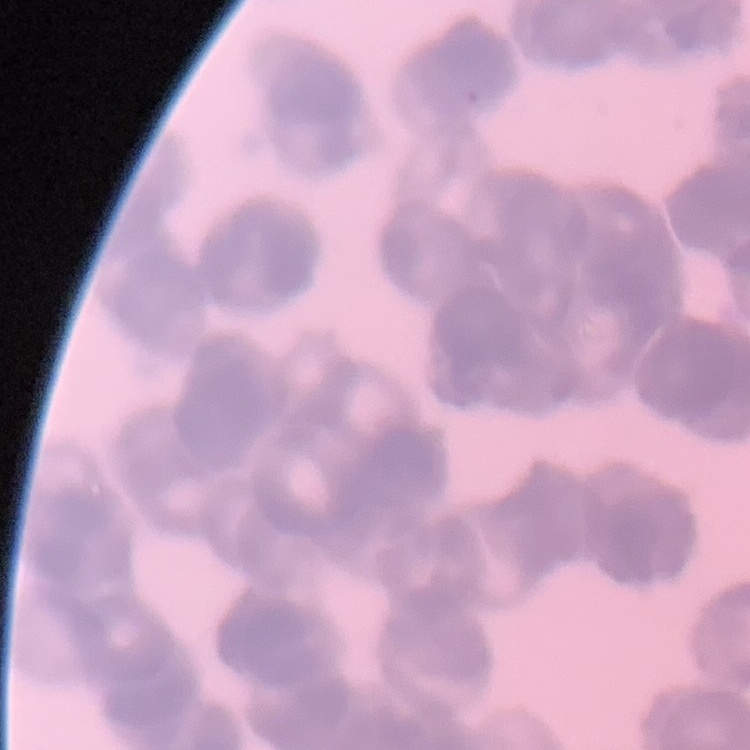
red_blood_cell_morphology: rouleaux formation
preparation: thin blood film
image_type: one tile cut from a larger photomicrograph
stain: Field's or Giemsa